Outline each blood parasite and name the species.
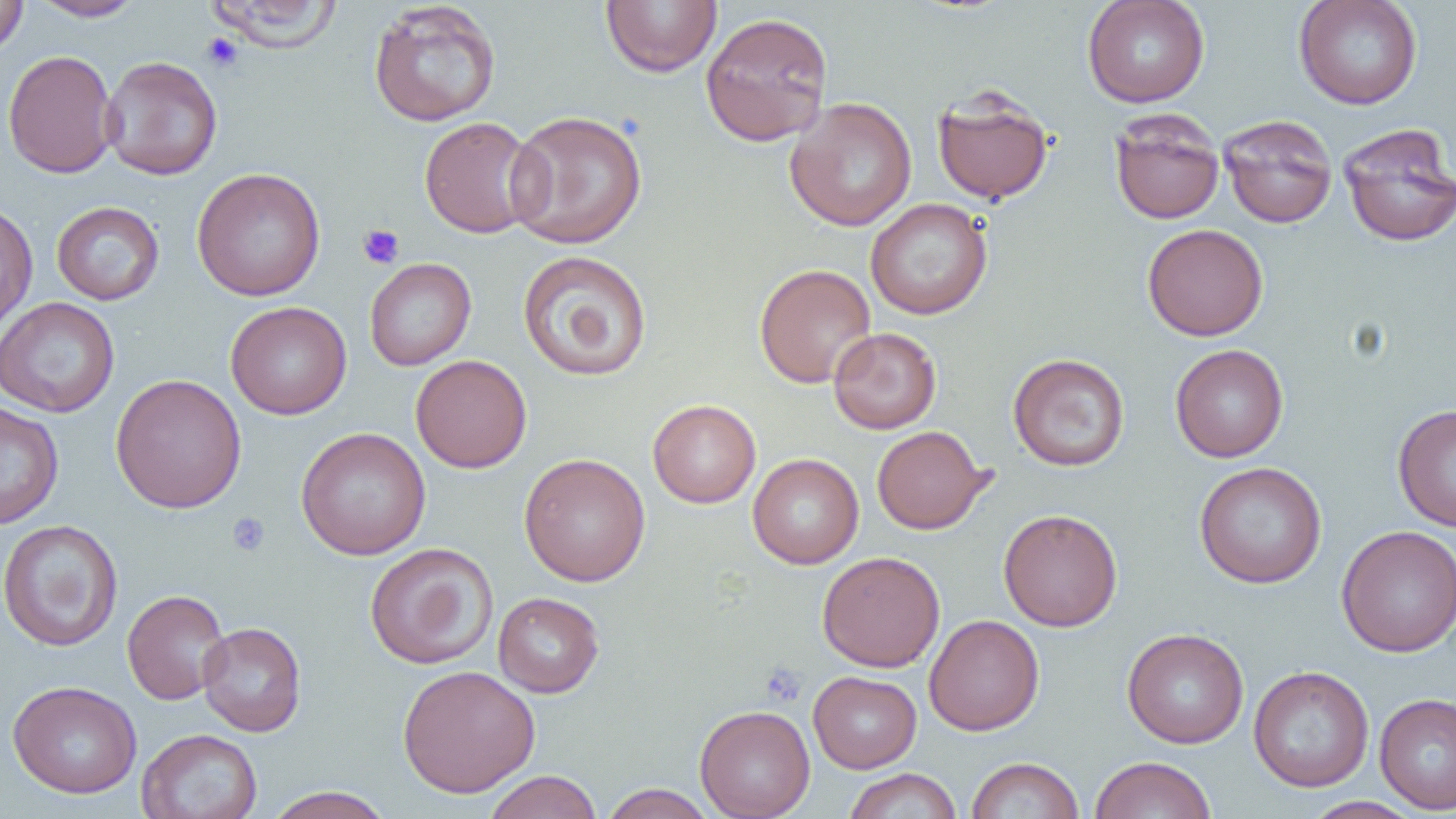

No blood parasites seen.

{
  "slide_level_diagnosis": "no evidence of blood parasites",
  "preparation": "thin blood film",
  "image_size": "1456×819 pixels",
  "uninfected_red_blood_cell_locations": "approximate bounding boxes as (x1,y1)-(x2,y2) corner pairs in pixels: (30,0)-(147,21), (203,0)-(344,52), (600,0)-(722,78), (1082,0)-(1210,108), (1293,0)-(1423,110), (0,1)-(28,58), (368,2)-(502,127), (700,11)-(834,147), (3,49)-(119,179), (100,56)-(223,181), (932,88)-(1055,205), (784,97)-(918,232), (505,110)-(648,250), (1109,112)-(1225,225), (1219,115)-(1338,228), (418,116)-(544,239), (1337,124)-(1456,247), (191,167)-(326,301), (865,198)-(993,320), (0,200)-(38,333), (51,201)-(164,305), (1142,223)-(1269,341), (517,250)-(653,382), (364,257)-(476,371), (754,263)-(877,388), (0,297)-(120,417), (225,301)-(351,420), (828,327)-(942,434), (1170,344)-(1289,462), (1007,353)-(1130,471), (410,354)-(532,473), (110,373)-(247,513), (647,399)-(761,508), (0,402)-(64,529), (1392,403)-(1456,531), (872,425)-(990,534), (295,427)-(431,560), (519,452)-(651,587), (748,453)-(864,569), (1193,461)-(1327,588), (998,508)-(1123,632), (0,519)-(124,651), (1336,525)-(1456,657), (364,542)-(499,670), (817,551)-(945,672), (122,588)-(231,705), (492,591)-(605,697), (924,614)-(1044,736), (197,622)-(307,736), (1122,627)-(1249,748), (397,665)-(540,798), (1248,665)-(1374,792), (808,671)-(921,773), (7,680)-(142,799), (1374,693)-(1456,814), (694,705)-(815,819), (136,728)-(263,819), (1089,755)-(1217,819), (966,756)-(1085,818), (843,768)-(962,819), (482,770)-(603,819), (598,783)-(716,819), (263,786)-(395,819), (1303,796)-(1424,818)",
  "field_of_view": "one of a larger specimen",
  "platelet_locations": "approximate bounding boxes as (x1,y1)-(x2,y2) corner pairs in pixels: (200,32)-(245,73), (357,224)-(404,269), (227,513)-(270,556), (760,663)-(806,706)",
  "modality": "light microscopy",
  "magnification": "1000x"
}